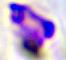
identification = white blood cell
modality = photomicrograph
magnification = 400x